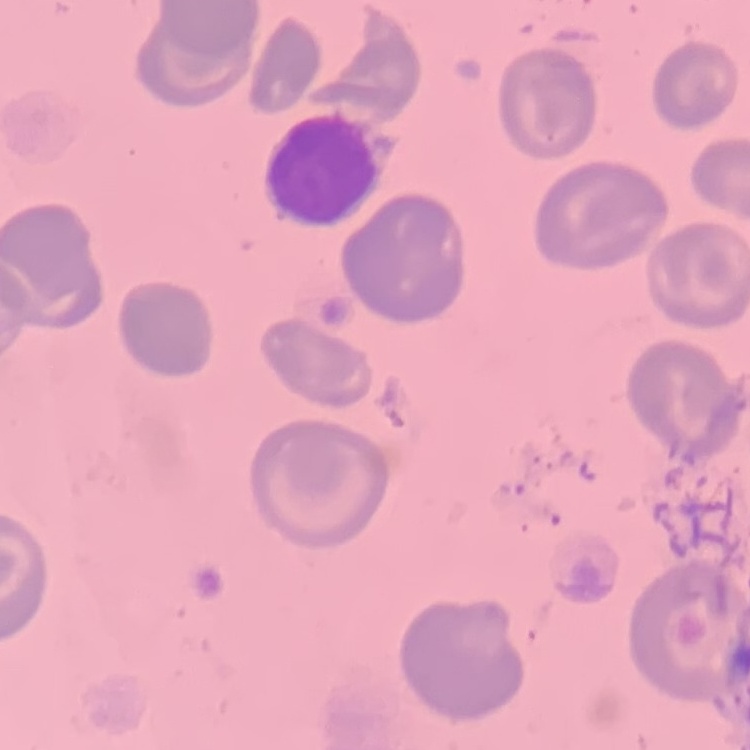
red blood cell morphology = no rouleaux formation
image type = square crop of a larger photomicrograph
stain = Field's or Giemsa
preparation = thin peripheral smear